Give the position of every Plasmodium parasite visible.
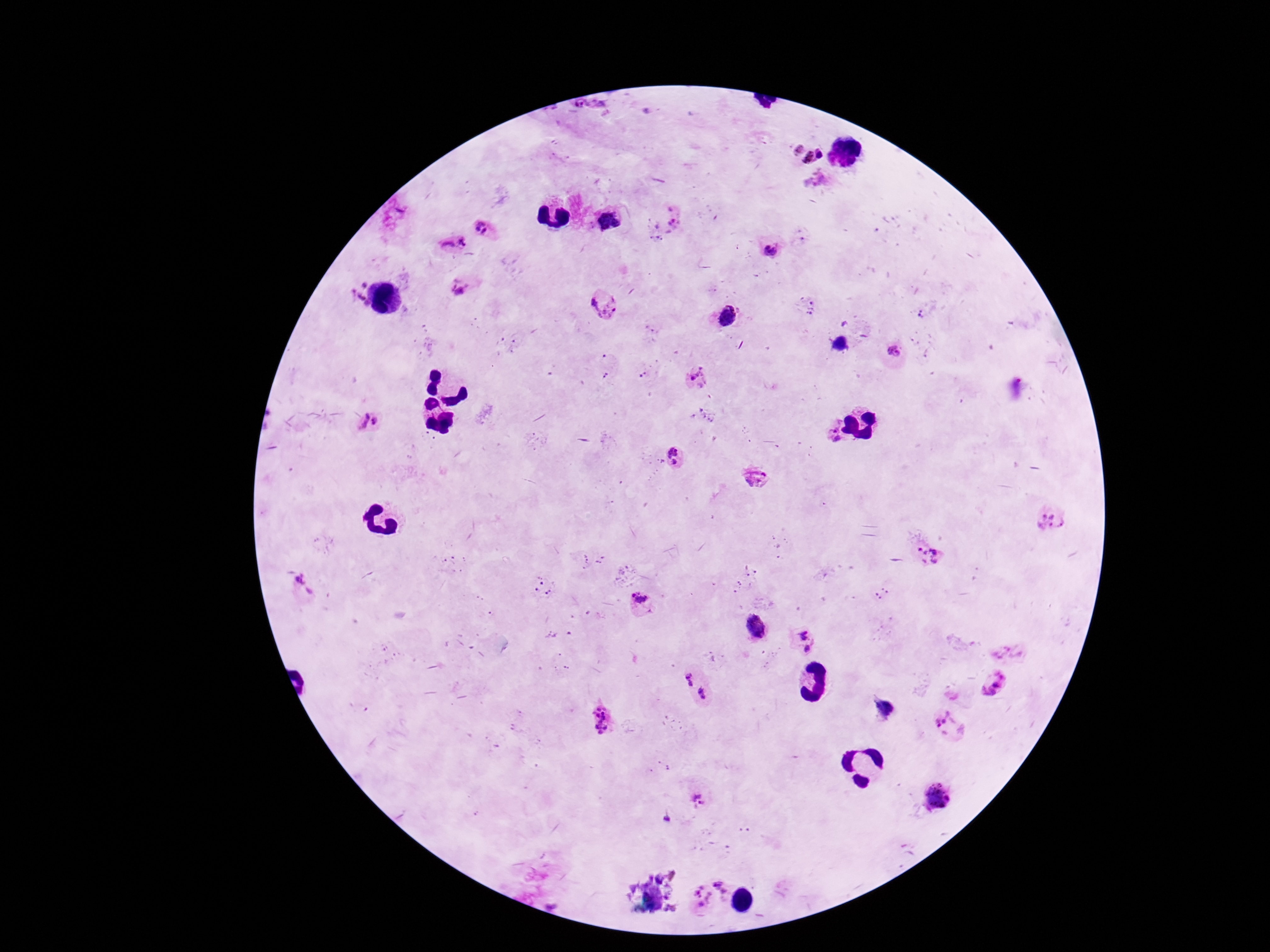
Approximate centers as [x, y] in pixels.
Plasmodium parasites: [808, 148], [674, 223], [485, 227], [453, 244], [770, 251], [461, 290], [358, 295], [603, 305], [893, 352], [699, 377], [366, 425], [830, 433], [676, 457], [761, 477], [1048, 518], [925, 553], [641, 605], [755, 629], [803, 639], [993, 684], [695, 685], [880, 707], [601, 719], [949, 725], [936, 798], [695, 801], [710, 896].

image size = 1270×952 pixels
stain = Giemsa
preparation = thick peripheral-blood smear
capture = smartphone camera through the microscope eyepiece
field of view = one from this slide
patient malaria status = positive
magnification = 100x